Identify the blood parasite species.
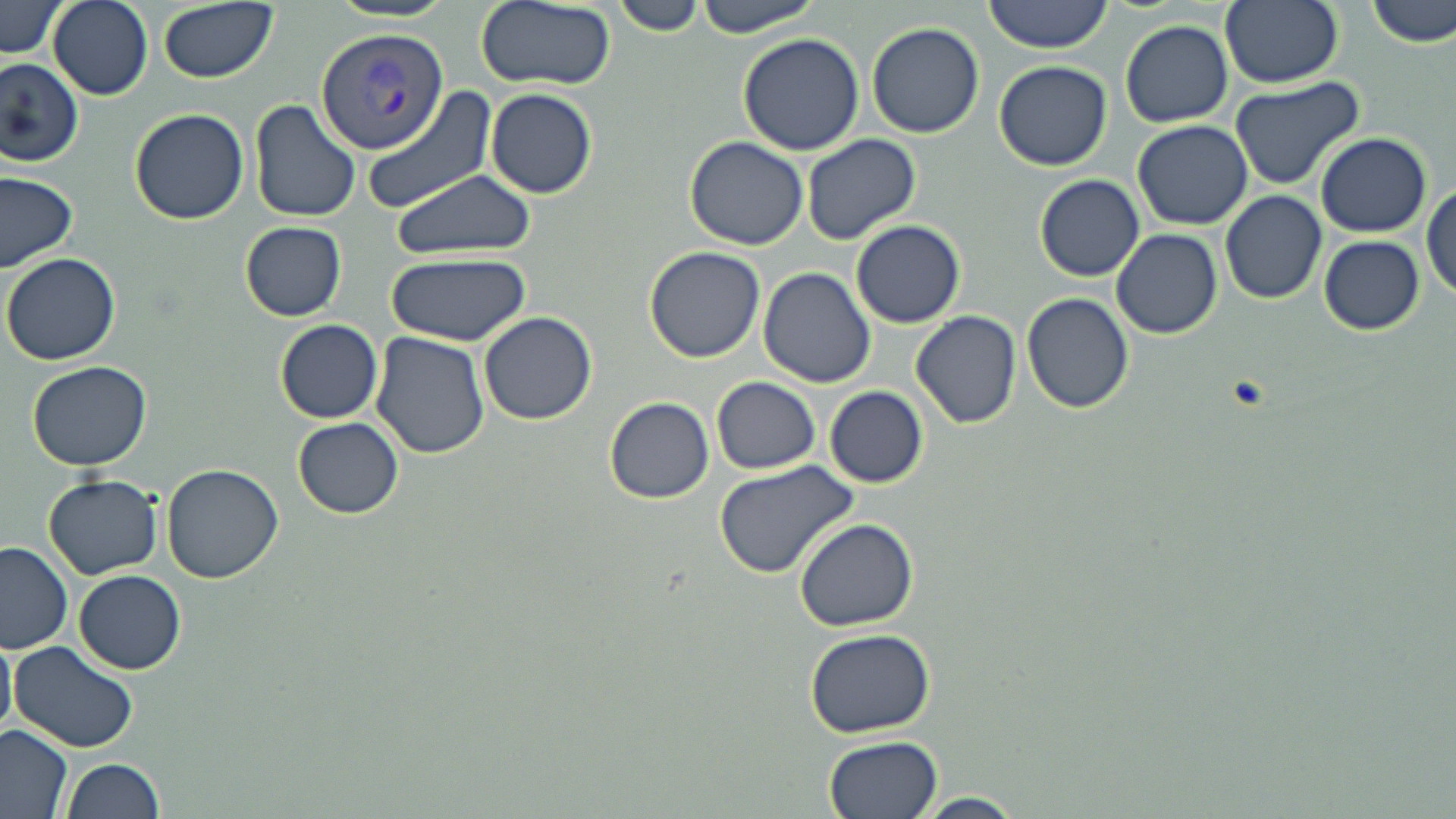
Plasmodium vivax.

Summary:
  - Coordinate format: approximate bounding boxes as (x1,y1)-(x2,y2) corner pairs in pixels
  - Plasmodium vivax-infected red blood cell locations: (316,26)-(448,154)
  - Uninfected red blood cell locations: (49,0)-(154,100), (155,0)-(277,83), (476,0)-(614,91), (613,0)-(704,37), (693,0)-(823,37), (983,0)-(1114,53), (1219,0)-(1343,89), (1368,0)-(1456,48), (0,1)-(67,60), (324,2)-(462,26), (1120,19)-(1233,127), (865,22)-(985,139), (738,34)-(867,156), (0,54)-(84,168), (993,61)-(1112,171), (1228,75)-(1367,190), (358,85)-(501,216), (486,88)-(597,199), (250,100)-(361,224), (128,107)-(249,225), (1133,120)-(1255,230), (1314,132)-(1431,237), (801,133)-(921,245), (685,137)-(809,249), (0,168)-(79,272), (385,170)-(540,260), (1035,174)-(1145,281), (1422,182)-(1456,300), (1221,190)-(1327,303), (850,219)-(967,328), (240,222)-(348,321), (1111,229)-(1222,340), (1318,235)-(1425,334), (644,246)-(765,363), (4,251)-(121,365), (386,252)-(530,346), (757,266)-(876,389), (1022,291)-(1134,414), (911,310)-(1022,429), (480,311)-(597,424), (275,319)-(384,423), (369,333)-(490,462), (26,359)-(153,470), (711,376)-(821,475), (825,386)-(929,488), (603,395)-(715,504), (294,418)-(403,519), (712,459)-(861,577), (161,463)-(283,583), (44,474)-(164,579), (795,518)-(918,632), (1,541)-(74,653), (74,570)-(186,674), (803,627)-(936,738), (0,631)-(17,738), (9,640)-(139,753), (0,725)-(76,818), (823,736)-(944,819), (61,757)-(167,819), (916,791)-(1026,818)
  - Preparation: thin blood film
  - Image size: 1456×819 pixels
  - Modality: light microscopy
  - Magnification: 1000x
  - Field of view: one of a larger specimen
  - Stain: May-Grünwald-Giemsa